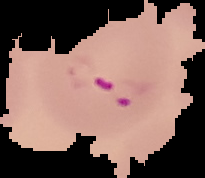
result = Plasmodium parasites detected
image size = 205×178 pixels
preparation = thin blood film
image type = segmented cell region on a black background